State which cell type is depicted.
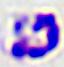

This is a leukocyte.

modality = photomicrograph
magnification = 400x